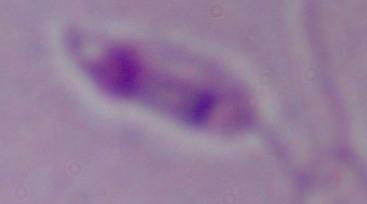
magnification = 1000x
identification = Leishmania
modality = micrograph